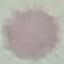
malaria status = uninfected
stain = Giemsa
capture = smartphone through the microscope eyepiece
preparation = thin blood film
image type = automatically extracted cell patch, resized to 64 × 64 pixels